Report the malaria status of this cell.
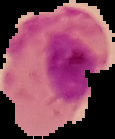

Parasitized.

Summary:
  - Preparation: thin blood smear
  - Image type: segmented cell region on a black background
  - Image size: 115×139 pixels